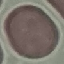
result = negative for malaria parasites
preparation = thin smear
capture = smartphone camera at the microscope eyepiece
stain = Giemsa
image type = cell patch, automatically extracted from a larger field of view and resized to 64 × 64 pixels